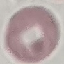

Summary:
  - Malaria status: uninfected
  - Preparation: thin blood film
  - Stain: Giemsa
  - Image type: automatically extracted cell patch, resized to 64 × 64 pixels
  - Capture: smartphone through the microscope eyepiece